Give the extent of all white blood cells.
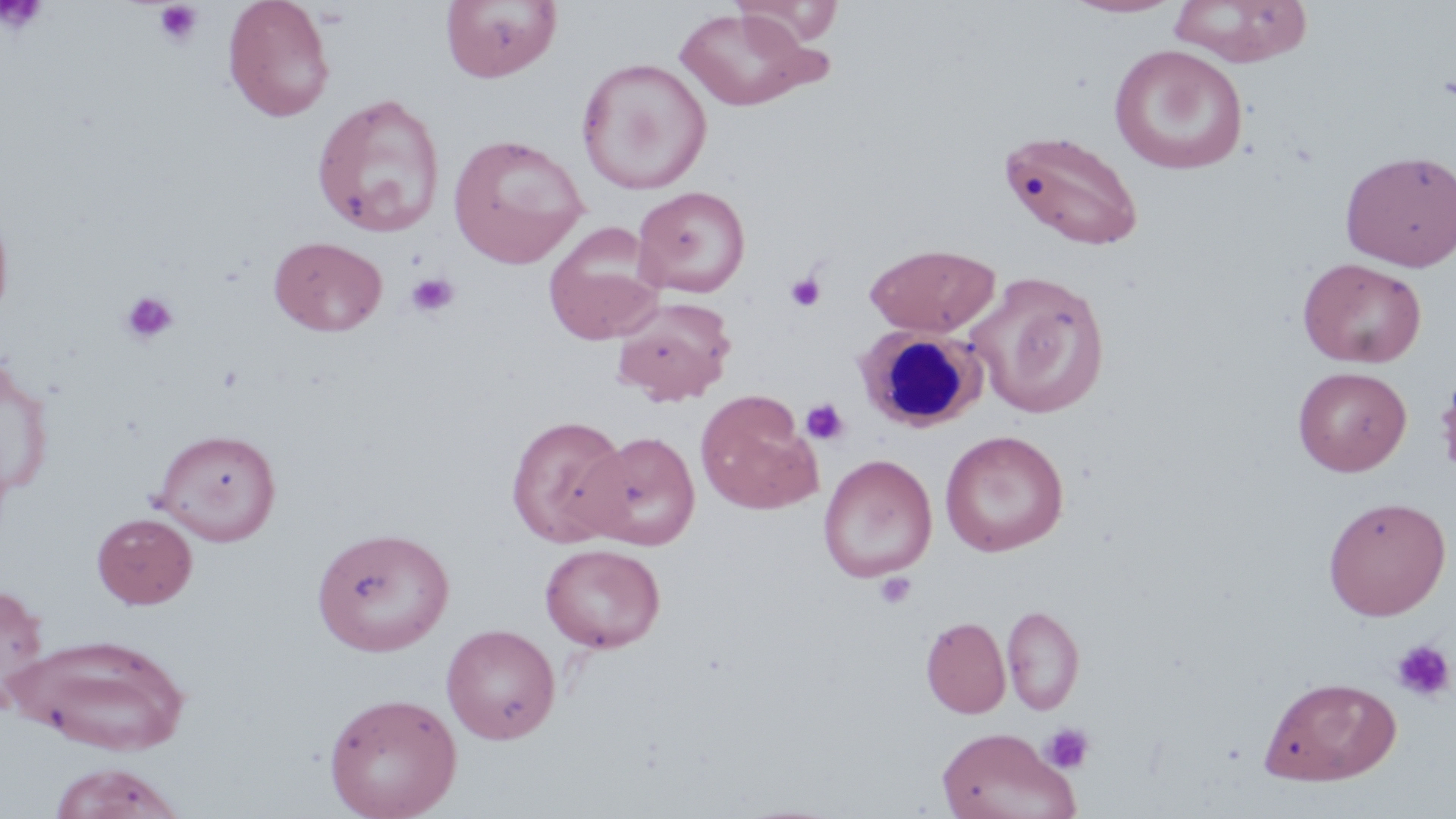
Approximate bounding boxes as (x1,y1)-(x2,y2) corner pairs in pixels.
White blood cells: (855,324)-(985,433).

Uninfected red blood cell locations: (222,0)-(335,122), (441,0)-(561,83), (1063,0)-(1182,18), (1169,0)-(1313,66), (732,1)-(843,46), (675,6)-(829,113), (1109,43)-(1248,175), (576,57)-(712,194), (310,92)-(446,238), (1001,129)-(1145,251), (447,133)-(590,268), (1340,150)-(1455,271), (632,185)-(751,299), (542,223)-(666,345), (268,235)-(387,337), (864,243)-(1000,337), (1298,257)-(1427,368), (966,270)-(1111,420), (611,298)-(735,405), (0,354)-(53,498), (1293,366)-(1412,476), (696,391)-(821,514), (505,414)-(632,547), (151,427)-(282,545), (940,430)-(1069,557), (582,431)-(700,550), (819,454)-(937,582), (1323,496)-(1451,620), (91,512)-(198,609), (311,526)-(455,656), (540,543)-(665,653), (0,582)-(50,709), (1002,604)-(1085,715), (921,617)-(1011,718), (441,624)-(560,744), (14,634)-(193,754), (1259,676)-(1401,785), (323,692)-(463,819), (935,727)-(1081,819), (46,762)-(186,819). Platelet locations: (154,2)-(203,47), (1,3)-(47,36), (405,272)-(460,318), (784,272)-(826,313), (119,290)-(180,346), (801,398)-(849,445), (874,572)-(917,610), (1391,638)-(1455,703), (1041,722)-(1095,774). Slide-level diagnosis: no evidence of blood parasites. Image is 1456×819 pixels. Captured at 1000x magnification. May-Grünwald-Giemsa-stained preparation. Light microscopy. Single field of view. Thin blood film.